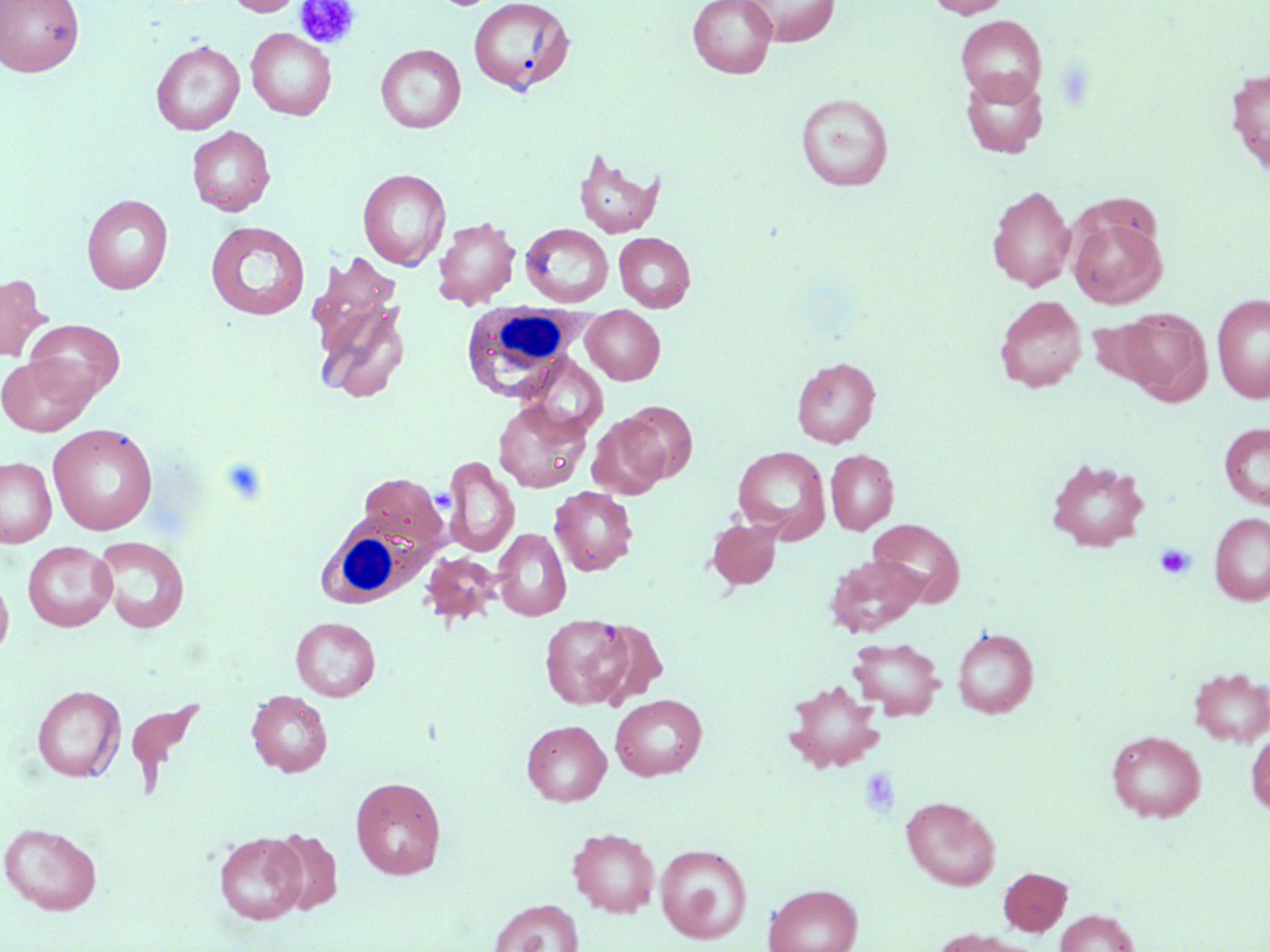
slide_level_diagnosis: no evidence of blood parasites
stain: May-Grünwald-Giemsa
uninfected_red_blood_cell_locations: 'approximate bounding boxes as named x1/y1/x2/y2 corners in pixels: (x1=0, y1=0, x2=84, y2=76), (x1=225, y1=0, x2=306, y2=16), (x1=434, y1=0, x2=506, y2=10), (x1=468, y1=0, x2=576, y2=96), (x1=688, y1=0, x2=777, y2=78), (x1=740, y1=0, x2=840, y2=47), (x1=927, y1=0, x2=1013, y2=18), (x1=955, y1=16, x2=1047, y2=104), (x1=246, y1=28, x2=336, y2=120), (x1=151, y1=41, x2=244, y2=135), (x1=376, y1=44, x2=466, y2=133), (x1=1225, y1=66, x2=1270, y2=176), (x1=960, y1=69, x2=1048, y2=158), (x1=795, y1=93, x2=893, y2=191), (x1=187, y1=126, x2=275, y2=216), (x1=573, y1=147, x2=664, y2=238), (x1=357, y1=168, x2=451, y2=271), (x1=987, y1=185, x2=1077, y2=291), (x1=82, y1=194, x2=173, y2=294), (x1=1068, y1=216, x2=1166, y2=309), (x1=433, y1=217, x2=520, y2=308), (x1=205, y1=221, x2=310, y2=320), (x1=521, y1=223, x2=613, y2=307), (x1=614, y1=232, x2=696, y2=312), (x1=306, y1=252, x2=402, y2=353), (x1=0, y1=274, x2=51, y2=361), (x1=1211, y1=293, x2=1270, y2=402), (x1=994, y1=295, x2=1086, y2=393), (x1=315, y1=297, x2=411, y2=404), (x1=581, y1=307, x2=665, y2=385), (x1=1116, y1=308, x2=1210, y2=402), (x1=1084, y1=316, x2=1164, y2=391), (x1=25, y1=319, x2=125, y2=401), (x1=0, y1=354, x2=95, y2=436), (x1=517, y1=354, x2=608, y2=439), (x1=791, y1=357, x2=880, y2=447), (x1=493, y1=399, x2=592, y2=493), (x1=617, y1=401, x2=697, y2=486), (x1=588, y1=414, x2=670, y2=499), (x1=1219, y1=423, x2=1270, y2=510), (x1=48, y1=424, x2=158, y2=535), (x1=733, y1=446, x2=830, y2=541), (x1=826, y1=450, x2=899, y2=534), (x1=442, y1=456, x2=520, y2=558), (x1=0, y1=457, x2=56, y2=548), (x1=1045, y1=457, x2=1150, y2=551), (x1=358, y1=473, x2=447, y2=555), (x1=549, y1=486, x2=638, y2=575), (x1=1209, y1=513, x2=1270, y2=606), (x1=706, y1=518, x2=782, y2=590), (x1=868, y1=518, x2=964, y2=606), (x1=493, y1=528, x2=571, y2=620), (x1=94, y1=536, x2=190, y2=633), (x1=23, y1=541, x2=117, y2=631), (x1=420, y1=552, x2=501, y2=627), (x1=826, y1=554, x2=928, y2=637), (x1=0, y1=573, x2=14, y2=662), (x1=540, y1=613, x2=634, y2=709), (x1=291, y1=616, x2=381, y2=701), (x1=589, y1=619, x2=667, y2=709), (x1=952, y1=627, x2=1038, y2=717), (x1=847, y1=637, x2=945, y2=719), (x1=1188, y1=666, x2=1270, y2=746), (x1=784, y1=679, x2=884, y2=772), (x1=32, y1=685, x2=125, y2=782), (x1=247, y1=690, x2=333, y2=777), (x1=610, y1=694, x2=707, y2=781), (x1=522, y1=720, x2=611, y2=805), (x1=1106, y1=730, x2=1206, y2=821), (x1=1246, y1=732, x2=1270, y2=815), (x1=350, y1=776, x2=446, y2=879), (x1=901, y1=796, x2=1000, y2=890), (x1=1, y1=822, x2=102, y2=915), (x1=567, y1=827, x2=660, y2=917), (x1=267, y1=828, x2=343, y2=915), (x1=214, y1=831, x2=307, y2=925), (x1=655, y1=844, x2=752, y2=943), (x1=998, y1=867, x2=1072, y2=935), (x1=763, y1=884, x2=863, y2=952), (x1=489, y1=899, x2=584, y2=952), (x1=1055, y1=909, x2=1139, y2=952), (x1=931, y1=929, x2=1033, y2=952)'
preparation: thin blood film
image_size: 1270×952 pixels
white_blood_cell_locations: 'approximate bounding boxes as named x1/y1/x2/y2 corners in pixels: (x1=465, y1=303, x2=588, y2=404), (x1=318, y1=510, x2=438, y2=607)'
modality: optical microscopy
magnification: 1000x
field_of_view: single
platelet_locations: 'approximate bounding boxes as named x1/y1/x2/y2 corners in pixels: (x1=296, y1=0, x2=360, y2=50), (x1=217, y1=456, x2=272, y2=507), (x1=1154, y1=543, x2=1196, y2=580), (x1=859, y1=767, x2=901, y2=817)'